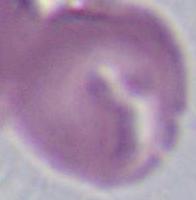
magnification = 1000x
modality = micrograph
identification = erythrocyte